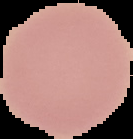

preparation = thin blood smear
image size = 133×139 pixels
image type = cell region segmented out of the field of view; surrounding area masked to black
malaria status = uninfected